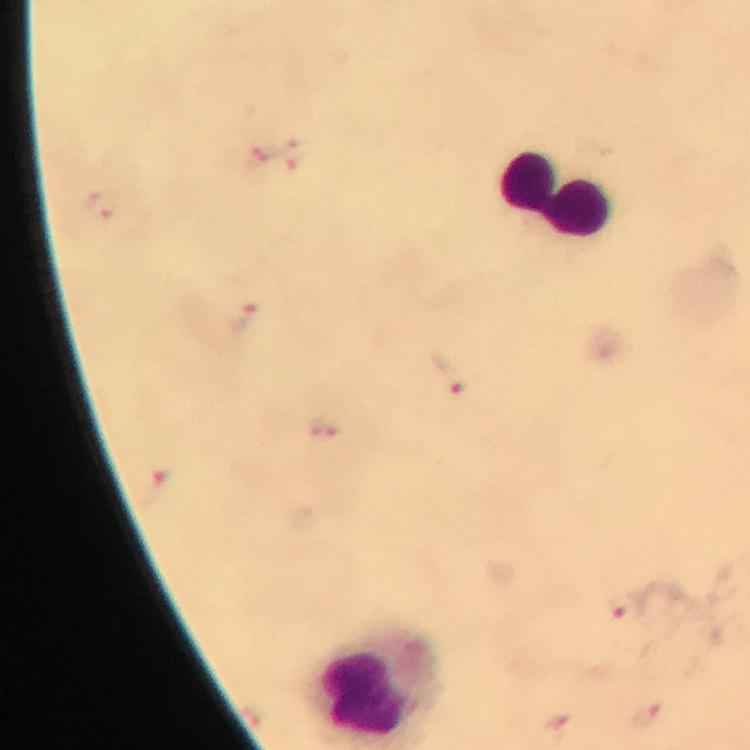
Approximate centers as {x, y} in pixels.
Summary:
  - Leukocyte locations: {557, 193}
  - Plasmodium parasite locations: {290, 155}, {258, 156}, {100, 204}, {242, 319}, {448, 374}, {325, 431}, {158, 487}, {622, 607}, {250, 716}, {648, 717}, {557, 729}
  - Immersion oil: used
  - Stain: Giemsa
  - Image size: 750×750 pixels
  - Context: from a diagnostic examination for malaria
  - Preparation: thick blood smear
  - Capture: smartphone camera through the microscope
  - Magnification: 100x
  - Cropped from: a single field of view